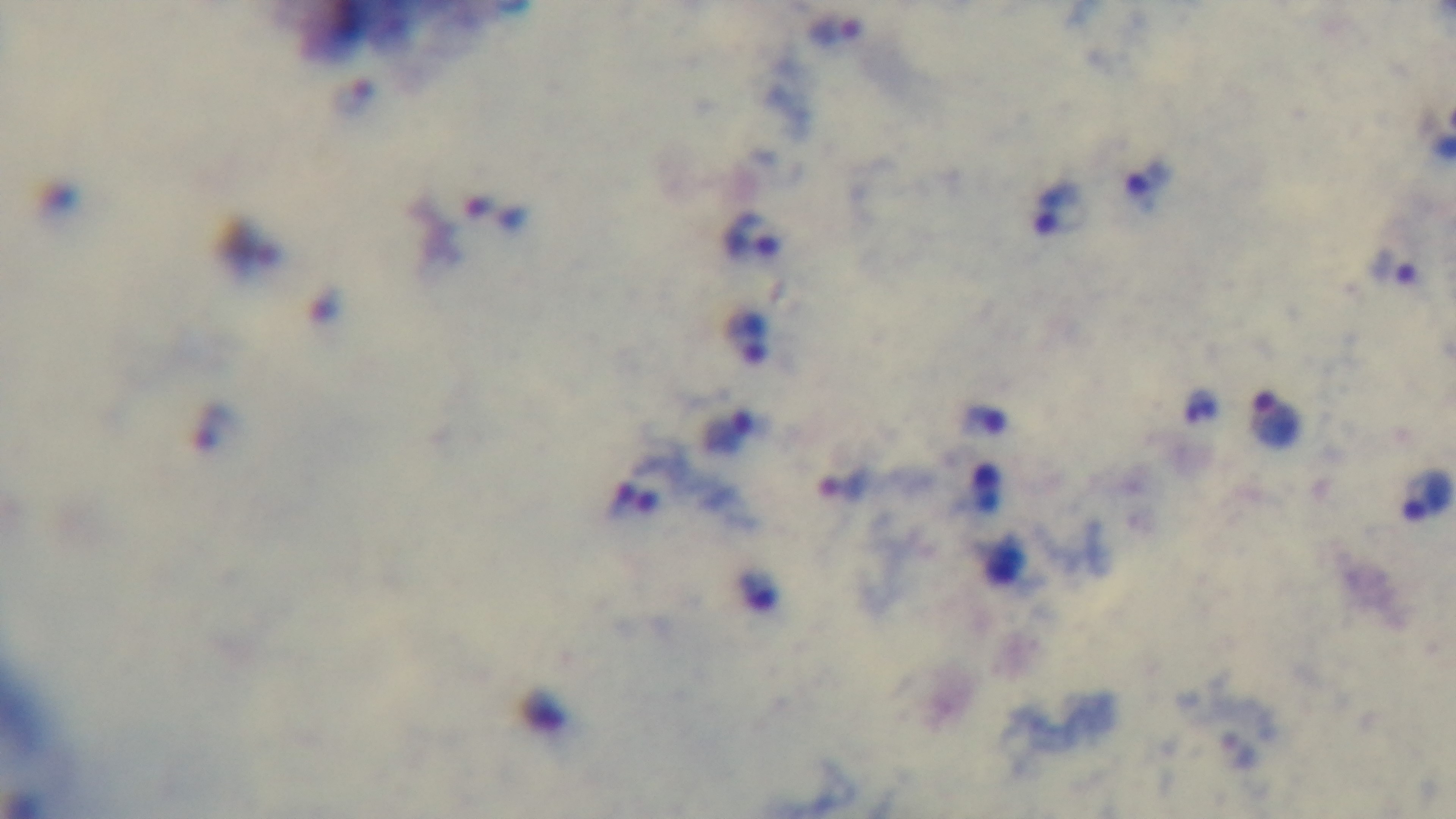
Malaria status: infected. Preparation: thick. Light microscopy. Mounted 4K digital camera. One field from the slide. Oil-immersion objective, 100x. Giemsa stain.